Assess this cell for malaria.
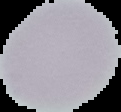

Uninfected.

image type = cell region segmented out of the field of view; surrounding area masked to black
preparation = thin blood film
image size = 121×112 pixels